Assess this cell for malaria.
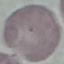
Uninfected.

stain: Giemsa
capture: smartphone camera at the microscope eyepiece
preparation: thin blood film
image_type: cell patch, automatically extracted from a larger field of view and resized to 64 × 64 pixels